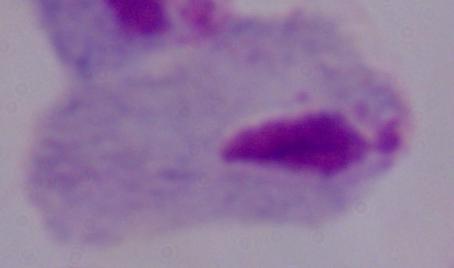

magnification = 1000x
identification = trichomonad
modality = micrograph